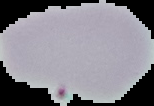
Summary:
  - Malaria status: uninfected
  - Image type: segmented cell region on a black background
  - Image size: 154×106 pixels
  - Preparation: thin blood smear